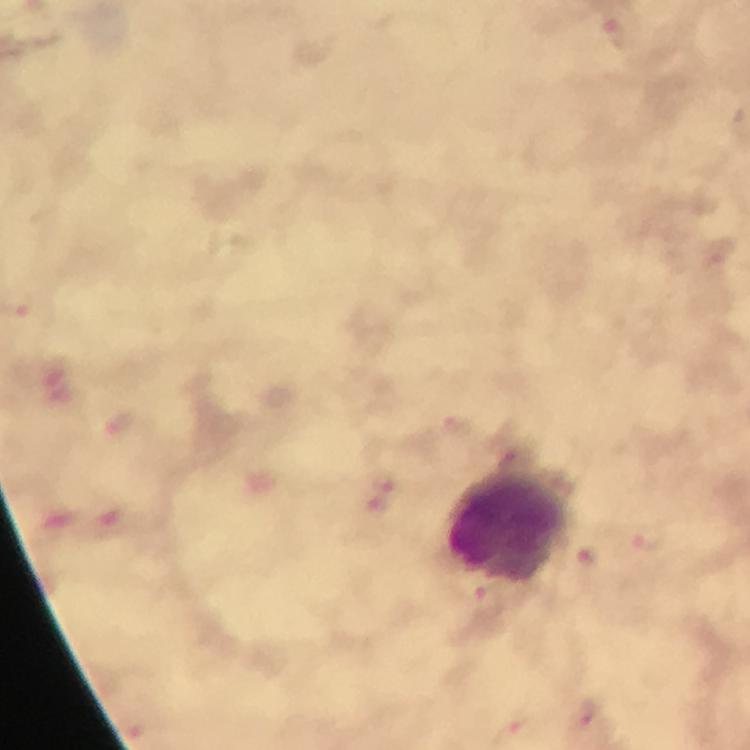

Approximate centers as (x, y) in pixels.
Summary:
  - Leukocyte locations: (510, 527)
  - Malaria parasite locations: (615, 34), (454, 427), (513, 460), (649, 541), (587, 558), (491, 605), (591, 720), (517, 728)
  - Immersion oil: applied
  - Image size: 750×750 pixels
  - Capture: smartphone mounted on the microscope
  - Context: from a diagnostic examination for malaria
  - Preparation: thick blood film
  - Cropped from: one field of view
  - Magnification: 100x
  - Stain: Giemsa